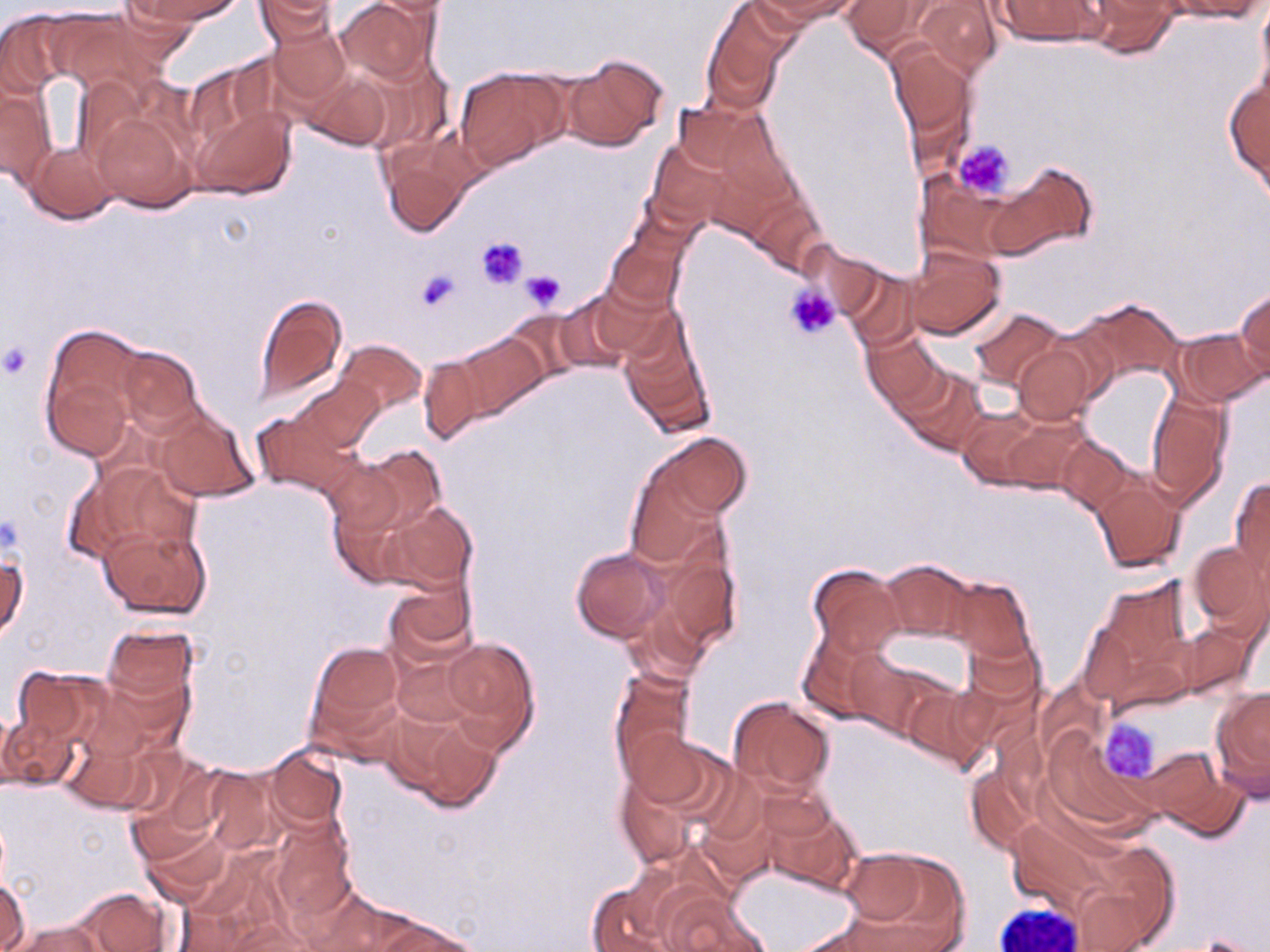

Approximate bounding boxes as (x1,y1)-(x2,y2) corner pairs in pixels. Uninfected red blood cell locations: (128,0)-(244,26), (337,0)-(438,86), (763,0)-(864,22), (840,0)-(934,58), (1161,0)-(1268,21), (1255,0)-(1270,102), (256,1)-(340,42), (911,1)-(1006,80), (993,1)-(1107,47), (1079,1)-(1181,58), (701,3)-(791,114), (0,10)-(72,96), (264,17)-(354,111), (886,42)-(976,150), (559,54)-(668,150), (303,65)-(394,151), (454,65)-(568,170), (1225,75)-(1270,187), (0,83)-(55,188), (670,99)-(776,185), (189,101)-(296,202), (89,107)-(198,213), (378,137)-(474,238), (646,140)-(731,230), (24,141)-(118,224), (986,165)-(1097,258), (919,172)-(1018,261), (604,235)-(686,314), (906,245)-(1006,342), (838,267)-(921,348), (581,281)-(676,363), (1235,287)-(1270,379), (550,292)-(640,374), (254,294)-(348,402), (1076,297)-(1185,386), (504,308)-(590,384), (969,308)-(1069,392), (618,316)-(715,439), (40,324)-(149,459), (1174,328)-(1265,405), (862,329)-(946,409), (448,334)-(547,424), (334,339)-(426,417), (1012,342)-(1097,426), (113,346)-(203,433), (416,353)-(491,444), (899,368)-(987,455), (291,377)-(384,455), (1146,387)-(1232,508), (152,406)-(256,503), (253,410)-(359,499), (956,410)-(1054,490), (643,432)-(752,530), (1054,435)-(1138,515), (343,445)-(446,549), (625,459)-(725,567), (73,462)-(199,562), (1091,474)-(1185,574), (1229,475)-(1270,583), (380,500)-(477,596), (99,523)-(211,619), (656,531)-(743,653), (1187,540)-(1269,636), (571,547)-(671,643), (1,549)-(27,643), (878,559)-(976,643), (806,562)-(906,657), (946,577)-(1034,662), (385,579)-(477,665), (1177,623)-(1257,699), (101,625)-(199,707), (796,628)-(891,723), (963,634)-(1044,717), (440,636)-(540,751), (310,642)-(402,734), (845,650)-(951,743), (390,655)-(477,731), (8,665)-(102,749), (609,667)-(694,779), (93,669)-(195,757), (901,684)-(992,773), (1210,686)-(1270,799), (728,696)-(835,796), (390,706)-(503,813), (0,709)-(22,793), (2,711)-(78,791), (60,723)-(155,814), (626,727)-(726,821), (263,747)-(347,833), (1140,748)-(1249,840), (123,757)-(226,866), (613,759)-(709,871), (199,765)-(278,858), (966,766)-(1038,853), (761,796)-(862,895), (697,805)-(779,889), (269,816)-(357,922), (1005,816)-(1121,924), (139,825)-(230,906), (1077,843)-(1181,950), (838,849)-(969,949), (0,876)-(29,952), (584,878)-(680,952), (305,885)-(423,952), (69,887)-(173,952), (659,891)-(769,952), (368,912)-(481,952), (216,918)-(320,952), (10,919)-(103,952). Platelet locations: (954,139)-(1014,198), (477,237)-(530,290), (415,267)-(461,315), (521,269)-(565,309), (785,284)-(840,342), (0,339)-(35,380), (1099,719)-(1161,782). Slide-level diagnosis: negative for blood parasites. Captured at 1000x magnification. Light microscopy. One field of a larger specimen. Image is 1270×952 pixels. May-Grünwald-Giemsa stain. Thin blood film.